Classify this cell by malaria status.
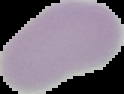

It is uninfected.

Image is 124×94 pixels. From a thin blood film. The area outside the segmented cell region is set to black.